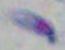 Photomicrograph. 1000x magnification. Toxoplasma gondii is shown.